Name the parasite shown.
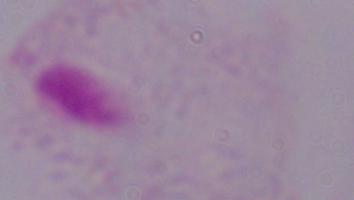

A trichomonad.

Summary:
  - Magnification: 1000x
  - Modality: photomicrograph